State the blood parasite species.
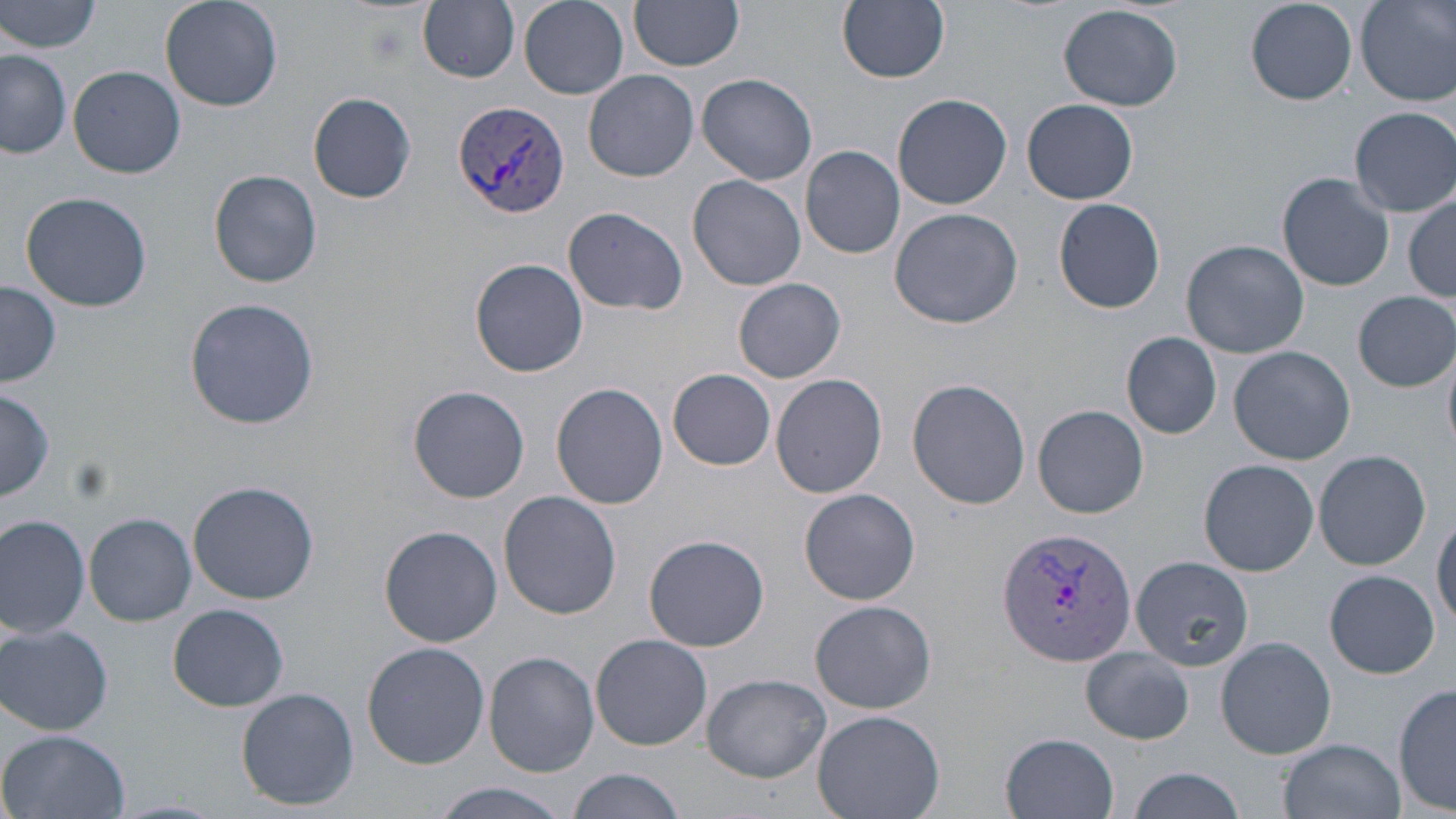
Plasmodium vivax.

Approximate bounding boxes as [x1, y1, x2, y2] in pixels. Plasmodium vivax-infected red blood cell locations: [453, 99, 571, 220], [998, 525, 1137, 667]. Uninfected red blood cell locations: [0, 0, 103, 55], [160, 0, 282, 112], [518, 0, 629, 98], [628, 0, 744, 71], [838, 0, 950, 84], [1245, 0, 1359, 105], [1356, 0, 1456, 104], [417, 1, 520, 83], [1058, 4, 1184, 111], [1, 50, 72, 159], [70, 65, 185, 178], [584, 69, 699, 182], [697, 72, 819, 185], [308, 91, 416, 203], [891, 93, 1012, 209], [1021, 98, 1139, 203], [1350, 106, 1456, 216], [800, 146, 906, 258], [209, 170, 322, 288], [1278, 172, 1395, 292], [687, 174, 807, 291], [1403, 188, 1455, 306], [21, 190, 152, 313], [1053, 196, 1167, 314], [563, 204, 691, 316], [889, 207, 1024, 329], [1180, 240, 1309, 358], [471, 258, 588, 377], [733, 277, 847, 384], [2, 280, 62, 388], [1353, 292, 1455, 391], [183, 297, 319, 431], [1121, 332, 1224, 438], [1442, 340, 1456, 456], [1228, 345, 1355, 464], [669, 369, 776, 469], [770, 374, 888, 499], [907, 378, 1031, 509], [552, 382, 668, 509], [407, 385, 530, 504], [0, 388, 53, 501], [1033, 403, 1150, 518], [1313, 449, 1432, 570], [1198, 459, 1319, 575], [188, 480, 320, 605], [798, 488, 922, 605], [498, 491, 621, 618], [1432, 511, 1456, 631], [84, 513, 196, 625], [0, 517, 90, 639], [379, 525, 503, 646], [644, 534, 769, 651], [1130, 555, 1253, 671], [1321, 571, 1441, 680], [809, 599, 936, 714], [167, 603, 289, 712], [1, 622, 114, 736], [590, 635, 712, 751], [1215, 637, 1336, 759], [362, 641, 490, 769], [1080, 646, 1196, 745], [483, 651, 599, 776], [700, 673, 832, 782], [1394, 679, 1455, 815], [237, 687, 359, 811], [811, 709, 944, 819], [0, 729, 129, 819], [1000, 732, 1119, 818], [1279, 736, 1405, 819], [568, 767, 690, 819], [1123, 767, 1247, 819], [428, 783, 570, 819]. Image is 1456×819 pixels. 1000x magnification. May-Grünwald-Giemsa stain. Optical microscopy. Thin blood film. Single field of view.